Locate and identify every blood parasite.
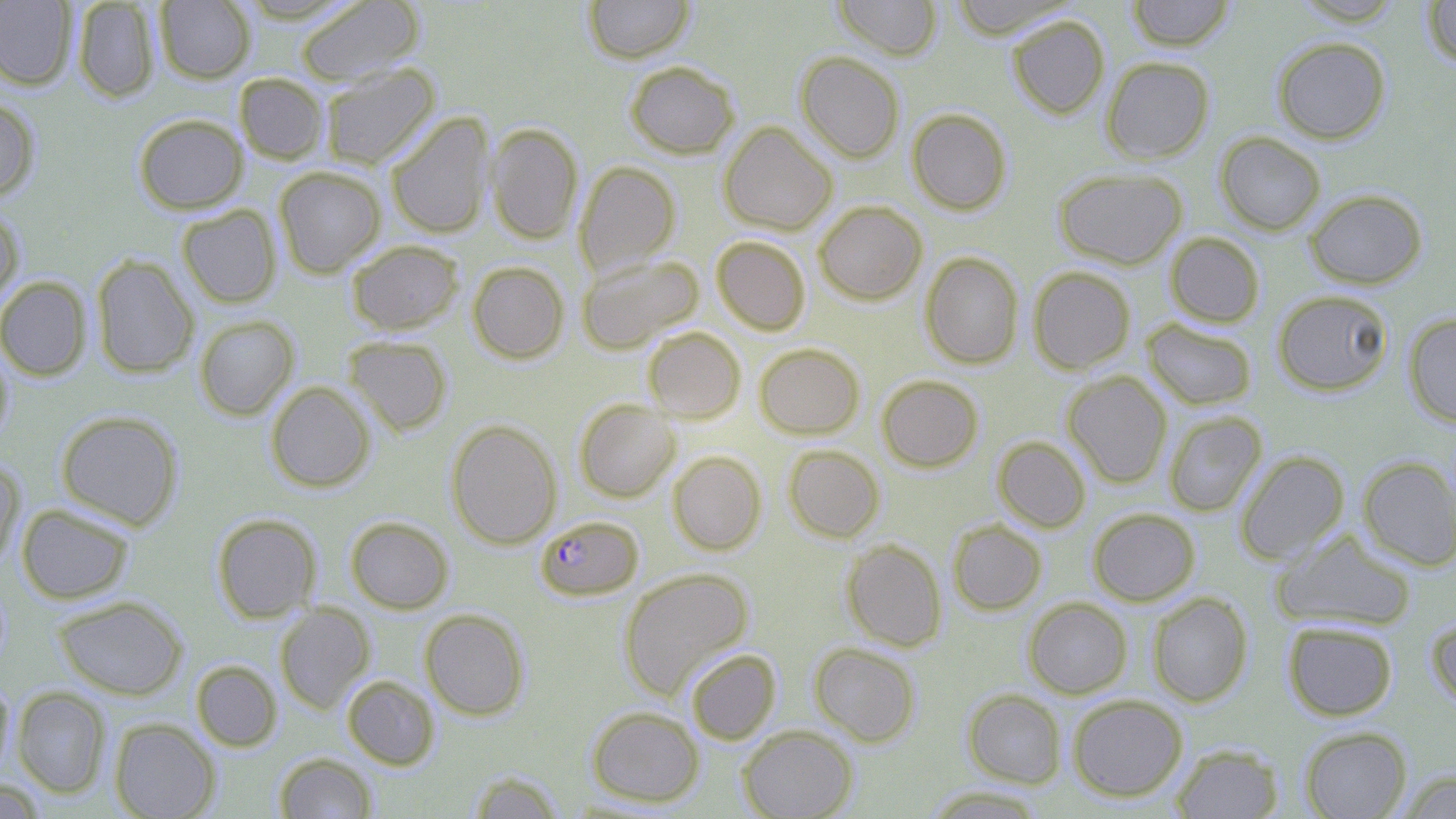

Approximate bounding boxes as [x1, y1, x2, y2] in pixels.
Plasmodium falciparum-infected red blood cells: [535, 515, 644, 602].
No Plasmodium ovale, Plasmodium malariae, Plasmodium vivax, Babesia divergens, or Trypanosoma brucei observed.

slide_level_diagnosis: Plasmodium falciparum
modality: light microscopy
stain: May-Grünwald-Giemsa
magnification: 1000x
preparation: thin blood smear
uninfected_red_blood_cell_locations: 'approximate bounding boxes as [x1, y1, x2, y2] in pixels: [72, 0, 159, 102], [154, 0, 255, 83], [294, 0, 425, 86], [583, 0, 694, 63], [833, 0, 942, 61], [948, 0, 1078, 39], [1126, 0, 1235, 51], [1291, 0, 1406, 25], [0, 1, 78, 90], [1421, 1, 1456, 67], [1007, 14, 1110, 120], [1271, 36, 1391, 144], [795, 51, 905, 163], [1101, 56, 1214, 164], [625, 61, 739, 159], [319, 63, 440, 170], [234, 73, 329, 164], [0, 96, 41, 201], [906, 108, 1012, 215], [385, 111, 495, 239], [133, 113, 248, 214], [719, 121, 837, 236], [486, 122, 584, 245], [1214, 131, 1326, 235], [574, 161, 681, 277], [274, 166, 386, 277], [1053, 167, 1188, 269], [1304, 188, 1427, 289], [814, 201, 927, 305], [177, 204, 282, 308], [0, 206, 24, 308], [1164, 232, 1265, 328], [712, 236, 811, 335], [346, 239, 464, 335], [920, 251, 1024, 370], [91, 254, 199, 378], [577, 254, 703, 354], [467, 261, 569, 363], [1028, 266, 1136, 375], [0, 276, 92, 381], [1271, 289, 1395, 396], [1403, 312, 1456, 427], [194, 314, 299, 421], [1142, 319, 1257, 410], [643, 327, 745, 423], [344, 336, 452, 435], [0, 341, 14, 446], [754, 343, 865, 439], [1062, 371, 1172, 488], [877, 374, 983, 472], [265, 381, 375, 492], [573, 398, 679, 503], [56, 409, 184, 530], [1163, 410, 1267, 517], [445, 419, 561, 548], [993, 436, 1091, 532], [783, 444, 885, 542], [668, 450, 767, 555], [1234, 451, 1349, 564], [1357, 456, 1456, 571], [0, 459, 25, 569], [17, 503, 134, 604], [1088, 507, 1200, 606], [211, 513, 322, 622], [346, 516, 454, 613], [947, 520, 1046, 615], [1272, 529, 1417, 631], [842, 539, 947, 651], [618, 567, 754, 700], [1147, 592, 1253, 707], [54, 595, 187, 700], [1023, 597, 1132, 699], [275, 604, 374, 713], [420, 608, 530, 720], [1425, 612, 1456, 712], [1283, 619, 1398, 720], [809, 642, 922, 746], [685, 648, 781, 744], [191, 660, 283, 751], [342, 675, 440, 769], [0, 677, 14, 783], [12, 686, 111, 797], [962, 689, 1067, 788], [1067, 694, 1187, 802], [586, 705, 704, 807], [109, 718, 220, 819], [738, 725, 857, 819], [1299, 726, 1412, 818], [1171, 743, 1284, 818], [274, 752, 378, 819], [1396, 769, 1456, 818], [467, 770, 565, 818], [1, 782, 47, 817], [923, 786, 1047, 818]'
field_of_view: one of a larger specimen
image_size: 1456×819 pixels